Classify this cell by malaria status.
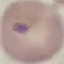
It is parasitized.

Acquired by smartphone through the microscope eyepiece. Thin blood film. Cell patch, automatically extracted from a larger field of view and resized to 64 × 64 pixels. Giemsa-stained preparation.